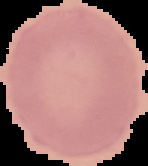
Summary:
  - Malaria status: uninfected
  - Image type: segmented cell region with the area outside set to black
  - Preparation: thin blood film
  - Image size: 148×166 pixels